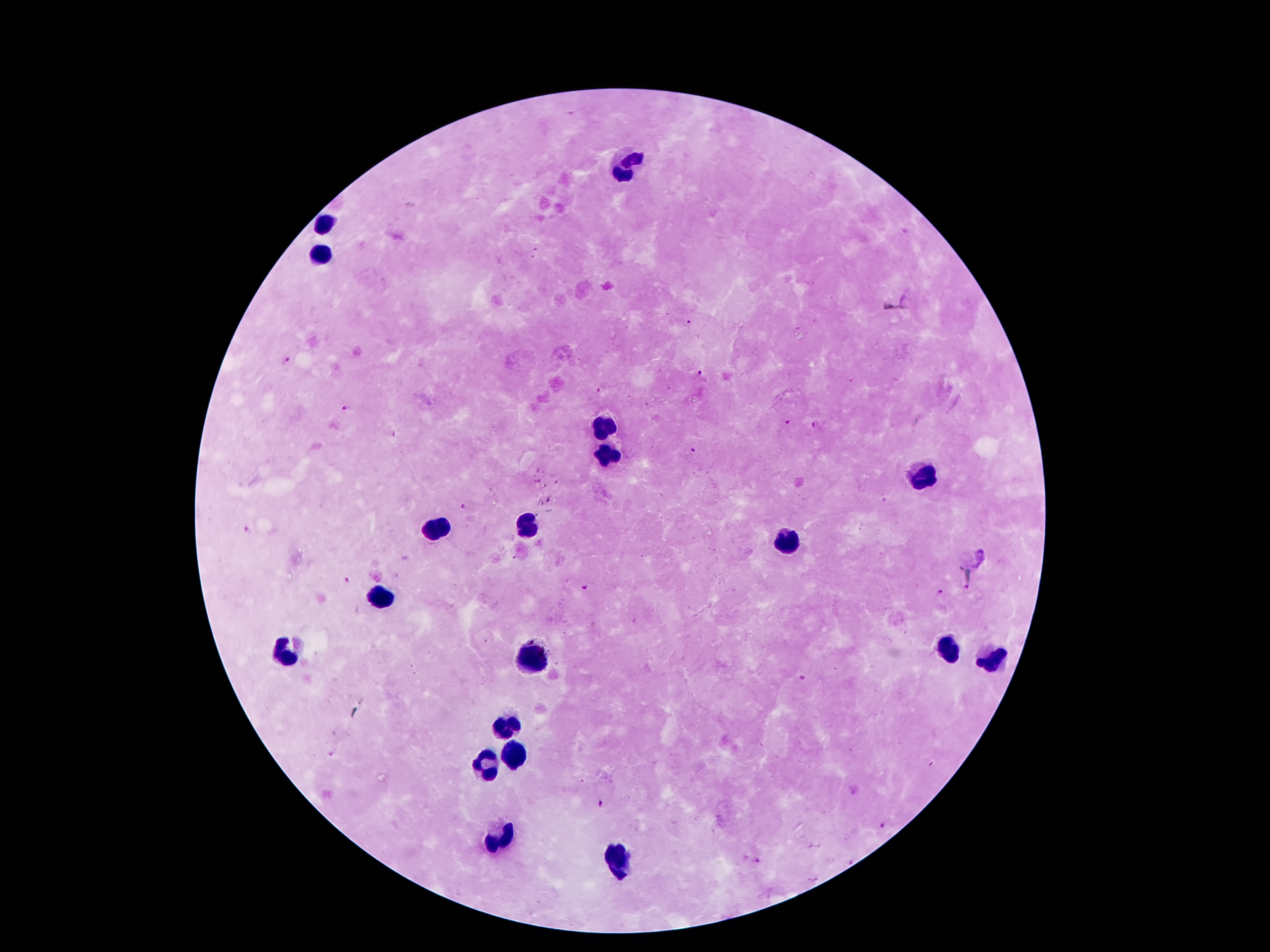
{
  "leukocyte_locations": "approximate object centers, in pixels from the top-left corner: (x=630, y=166), (x=326, y=225), (x=321, y=252), (x=603, y=428), (x=605, y=455), (x=924, y=479), (x=435, y=527), (x=527, y=527), (x=785, y=542), (x=378, y=596), (x=947, y=646), (x=288, y=653), (x=533, y=659), (x=991, y=659), (x=504, y=728), (x=512, y=758), (x=487, y=764), (x=500, y=840), (x=624, y=863)",
  "capture": "smartphone through the microscope eyepiece",
  "stain": "Giemsa",
  "image_size": "1270×952 pixels",
  "malaria_parasite_locations": "approximate object centers, in pixels from the top-left corner: (x=689, y=322), (x=287, y=361), (x=701, y=372), (x=599, y=390), (x=345, y=409), (x=788, y=423), (x=815, y=425), (x=693, y=452), (x=462, y=506), (x=246, y=529), (x=513, y=558), (x=346, y=579), (x=967, y=587), (x=584, y=588), (x=940, y=592), (x=802, y=678), (x=601, y=804), (x=884, y=824), (x=757, y=859)",
  "magnification": "100x",
  "preparation": "thick blood film",
  "field_of_view": "one from this slide",
  "patient_malaria_status": "positive for Plasmodium falciparum"
}